Identify the parasite.
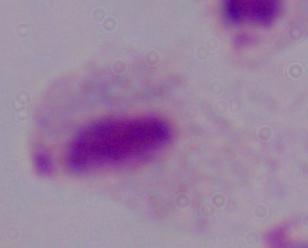

A trichomonad.

Captured at 1000x magnification. Micrograph.